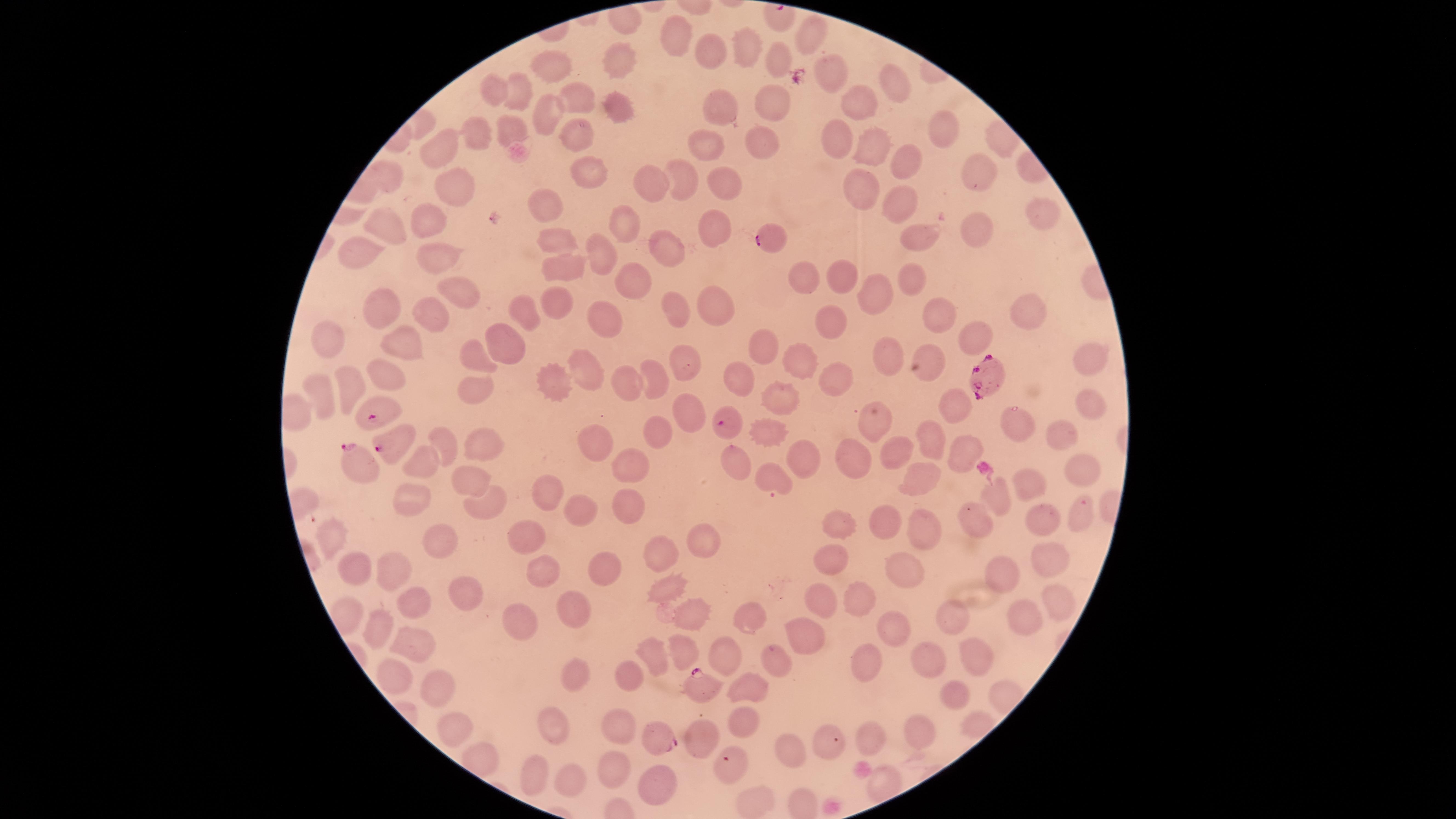

{
  "field_of_view": "single",
  "visible_region": "circular",
  "parasitized_red_blood_cells": "approximate marker points, in pixels from the top-left corner: (x=770, y=238), (x=981, y=375), (x=376, y=412), (x=729, y=419), (x=392, y=446), (x=355, y=459), (x=701, y=689), (x=657, y=738), (x=729, y=766)",
  "species": "Plasmodium falciparum",
  "image_size": "1456×819 pixels",
  "uninfected_red_blood_cells": "approximate marker points, in pixels from the top-left corner: (x=806, y=33), (x=674, y=37), (x=709, y=49), (x=744, y=49), (x=779, y=57), (x=615, y=63), (x=552, y=68), (x=831, y=74), (x=893, y=77), (x=493, y=90), (x=516, y=93), (x=576, y=98), (x=770, y=99), (x=855, y=103), (x=617, y=106), (x=721, y=106), (x=549, y=109), (x=504, y=125), (x=941, y=128), (x=569, y=133), (x=833, y=135), (x=474, y=136), (x=706, y=139), (x=762, y=140), (x=873, y=147), (x=440, y=150), (x=904, y=159), (x=589, y=166), (x=977, y=170), (x=651, y=176), (x=678, y=178), (x=857, y=185), (x=454, y=186), (x=724, y=187), (x=900, y=202), (x=543, y=203), (x=1038, y=214), (x=425, y=217), (x=617, y=222), (x=714, y=224), (x=974, y=225), (x=387, y=227), (x=917, y=233), (x=557, y=235), (x=666, y=245), (x=361, y=251), (x=600, y=251), (x=436, y=253), (x=559, y=267), (x=847, y=275), (x=802, y=276), (x=627, y=279), (x=907, y=279), (x=457, y=286), (x=875, y=295), (x=550, y=299), (x=380, y=304), (x=674, y=307), (x=718, y=307), (x=935, y=307), (x=527, y=308), (x=1026, y=314), (x=433, y=318), (x=601, y=319), (x=835, y=321), (x=966, y=329), (x=331, y=340), (x=408, y=342), (x=758, y=343), (x=498, y=344), (x=890, y=351), (x=474, y=356), (x=801, y=356), (x=1086, y=357), (x=684, y=358), (x=584, y=366), (x=924, y=370), (x=657, y=372), (x=383, y=374), (x=738, y=374), (x=836, y=376), (x=348, y=380), (x=550, y=383), (x=626, y=385), (x=474, y=388), (x=323, y=392), (x=786, y=395), (x=1089, y=401), (x=957, y=405), (x=688, y=413), (x=1019, y=417), (x=872, y=419), (x=762, y=428), (x=1067, y=433), (x=656, y=435), (x=929, y=437), (x=604, y=441), (x=447, y=442), (x=487, y=445), (x=890, y=451), (x=970, y=454), (x=794, y=455), (x=425, y=459), (x=631, y=460), (x=852, y=460), (x=739, y=461), (x=1078, y=467), (x=916, y=473), (x=770, y=477), (x=470, y=481), (x=1028, y=483), (x=546, y=493), (x=486, y=500), (x=995, y=500), (x=410, y=503), (x=624, y=505), (x=580, y=512), (x=1080, y=514), (x=975, y=520), (x=1040, y=521), (x=881, y=522), (x=836, y=523), (x=923, y=528), (x=527, y=537), (x=327, y=539), (x=436, y=539), (x=701, y=542), (x=1045, y=555), (x=664, y=556), (x=832, y=563), (x=608, y=564), (x=354, y=570), (x=548, y=571), (x=905, y=571), (x=391, y=573), (x=999, y=573), (x=665, y=587), (x=463, y=596), (x=855, y=597), (x=412, y=602), (x=1053, y=602), (x=823, y=604), (x=573, y=613), (x=685, y=615), (x=745, y=618), (x=517, y=619), (x=949, y=620), (x=1023, y=620), (x=376, y=626), (x=894, y=630), (x=800, y=636), (x=415, y=639), (x=729, y=648), (x=976, y=651), (x=684, y=652), (x=660, y=654), (x=782, y=660), (x=932, y=662), (x=867, y=663), (x=396, y=675), (x=622, y=675), (x=572, y=679), (x=743, y=685), (x=439, y=689), (x=956, y=692), (x=623, y=723), (x=741, y=727), (x=449, y=728), (x=923, y=729), (x=555, y=735), (x=871, y=736), (x=699, y=737), (x=782, y=750), (x=608, y=765), (x=532, y=772), (x=576, y=784), (x=660, y=784), (x=751, y=798)",
  "preparation": "thin smear of blood",
  "presence": "malaria parasites identified",
  "stain": "Giemsa",
  "capture": "smartphone photograph through the microscope eyepiece"
}